Point out each Plasmodium parasite.
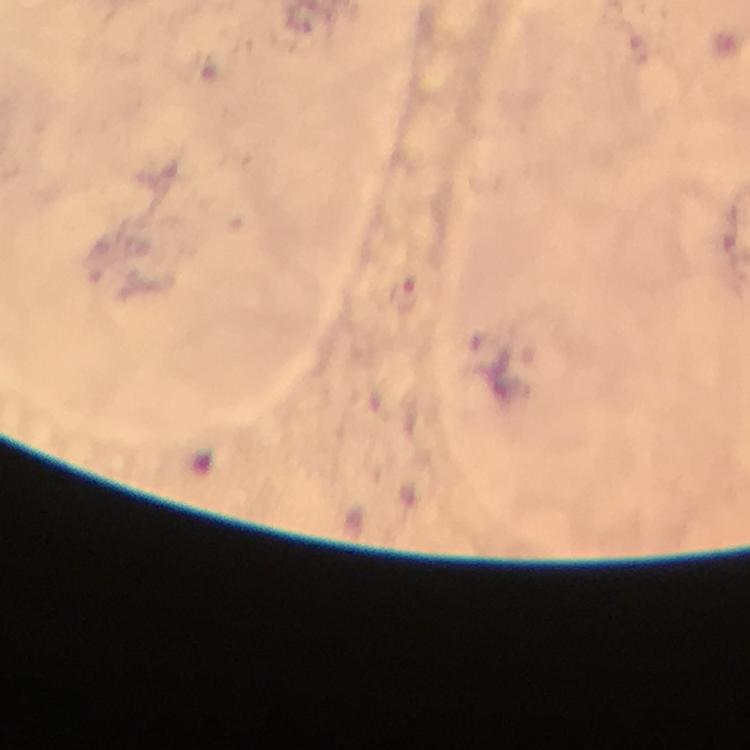

Approximate centers as {x, y} in pixels.
Plasmodium parasites: {405, 292}.

immersion oil = used
context = from a malaria diagnostic workup
magnification = 100x
image size = 750×750 pixels
preparation = thick blood smear
capture = smartphone mounted on the microscope
cropped from = one field of view
stain = Giemsa